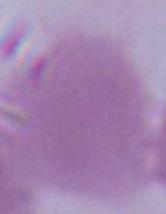

Summary:
  - Modality: micrograph
  - Magnification: 1000x
  - Identification: red blood cell